Outline every leukocyte.
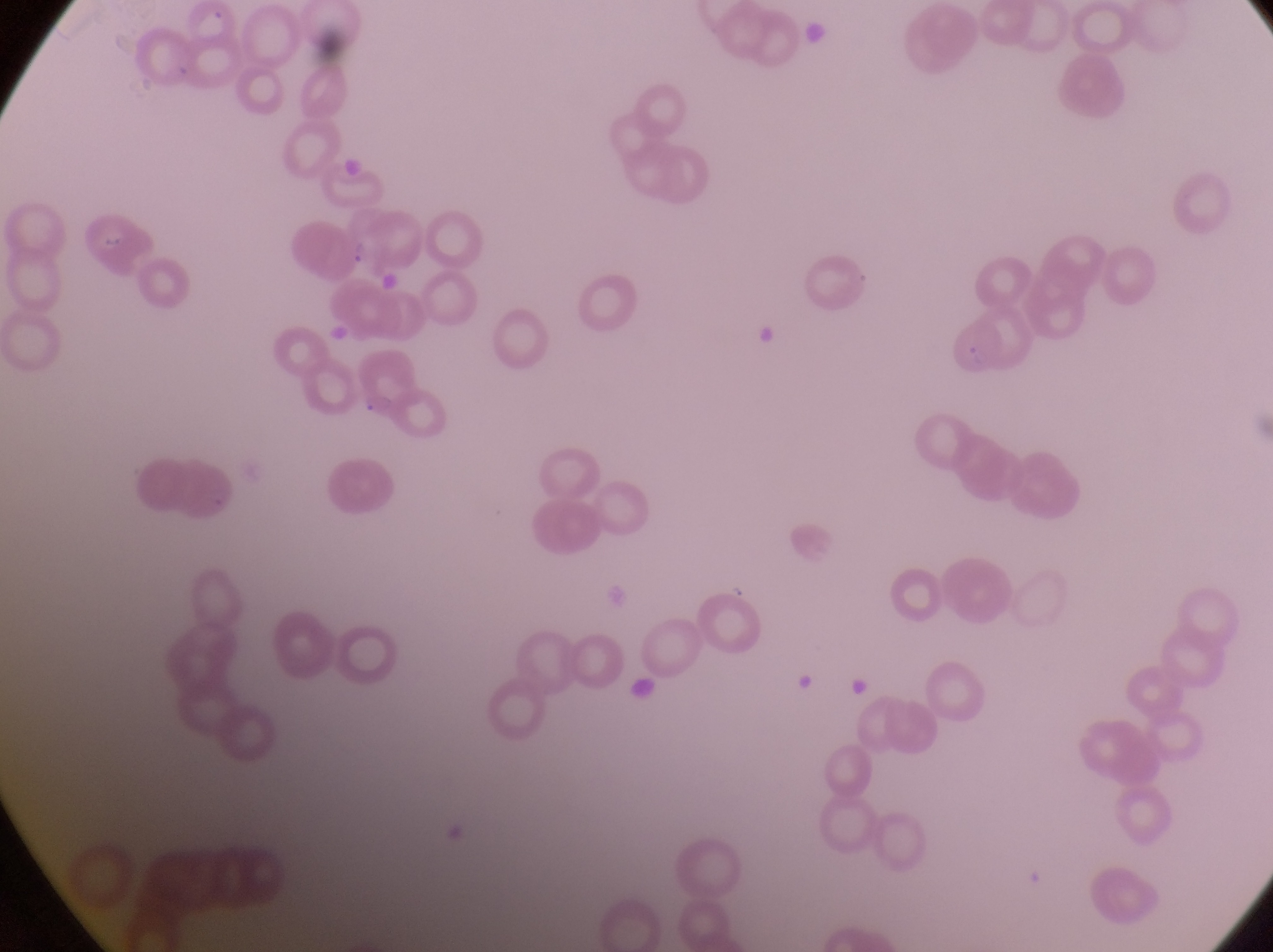
No leukocytes observed.

Approximate bounding boxes as [left, top, right, bottom] in pixels. Parasitised red blood cell locations: [340, 202, 398, 280]. Artifact (platelet-like body, stain precipitate, or debris) locations: [803, 19, 834, 47], [744, 318, 776, 348], [795, 673, 819, 696], [630, 678, 661, 709], [846, 678, 874, 699]. Thin blood smear. Image is 1273×952 pixels. One field of view. Photographed through the eyepiece of an Olympus CX-23 microscope with a smartphone camera. At a magnification of 1000x. Sample from Uganda.